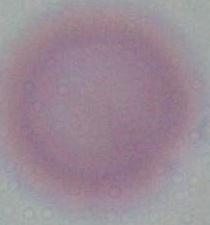
identification = red blood cell
modality = photomicrograph
magnification = 1000x